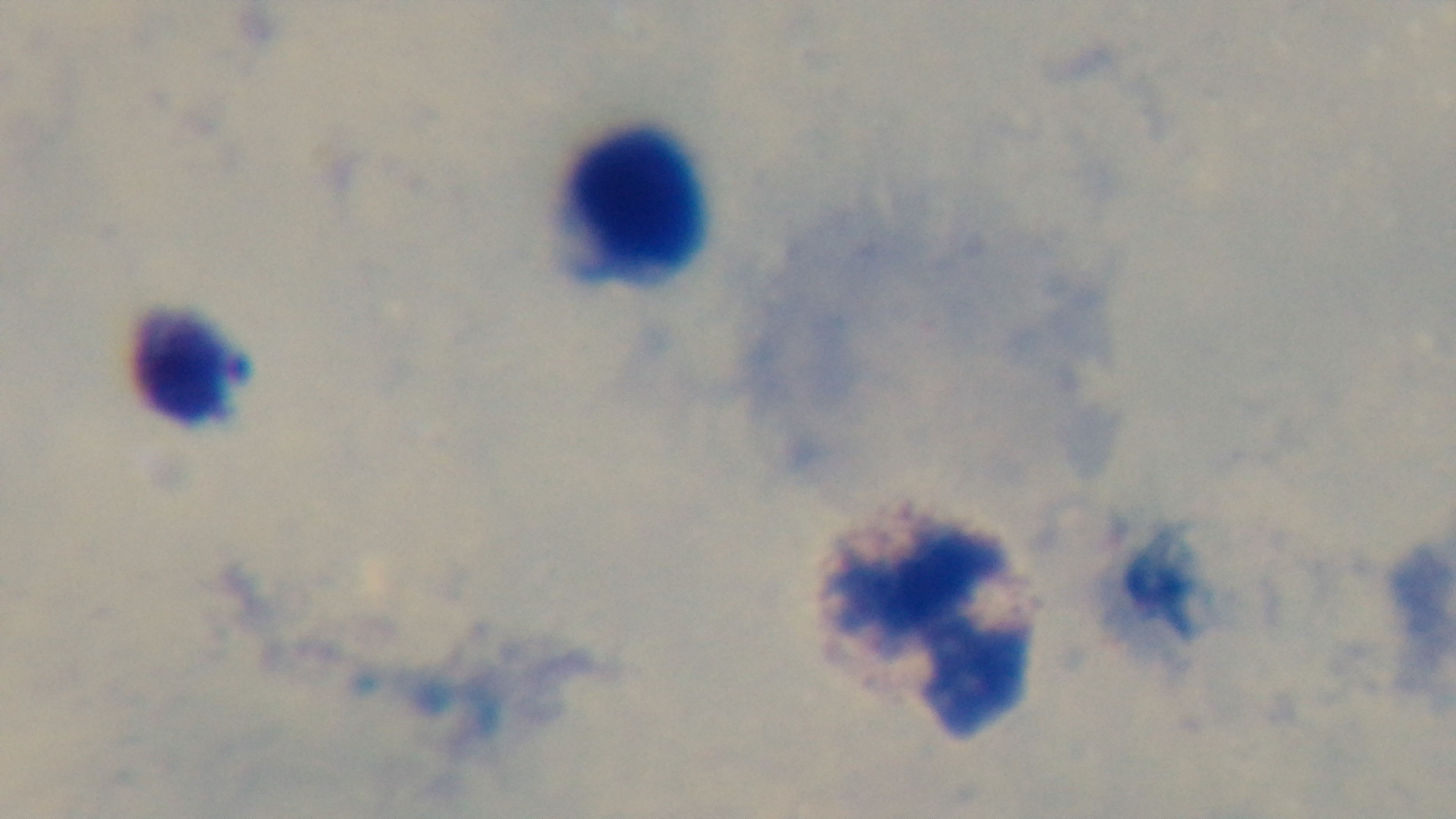
Summary:
  - Stain: Giemsa
  - Preparation: thick smear
  - Modality: light microscopy
  - Field of view: one from the slide
  - Objective: 100x oil immersion
  - Malaria status: uninfected
  - Capture: mounted 4K digital camera